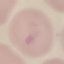
Summary:
  - Result: no malaria parasites detected
  - Preparation: thin blood film
  - Capture: smartphone through the microscope eyepiece
  - Image type: cell patch, automatically extracted from a larger field of view and resized to 64 × 64 pixels
  - Stain: Giemsa